Classify this cell by malaria status.
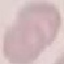
Uninfected.

Cell patch, automatically extracted from a larger field of view and resized to 64 × 64 pixels. Thin blood film. Giemsa-stained preparation. Acquired by smartphone through the microscope eyepiece.